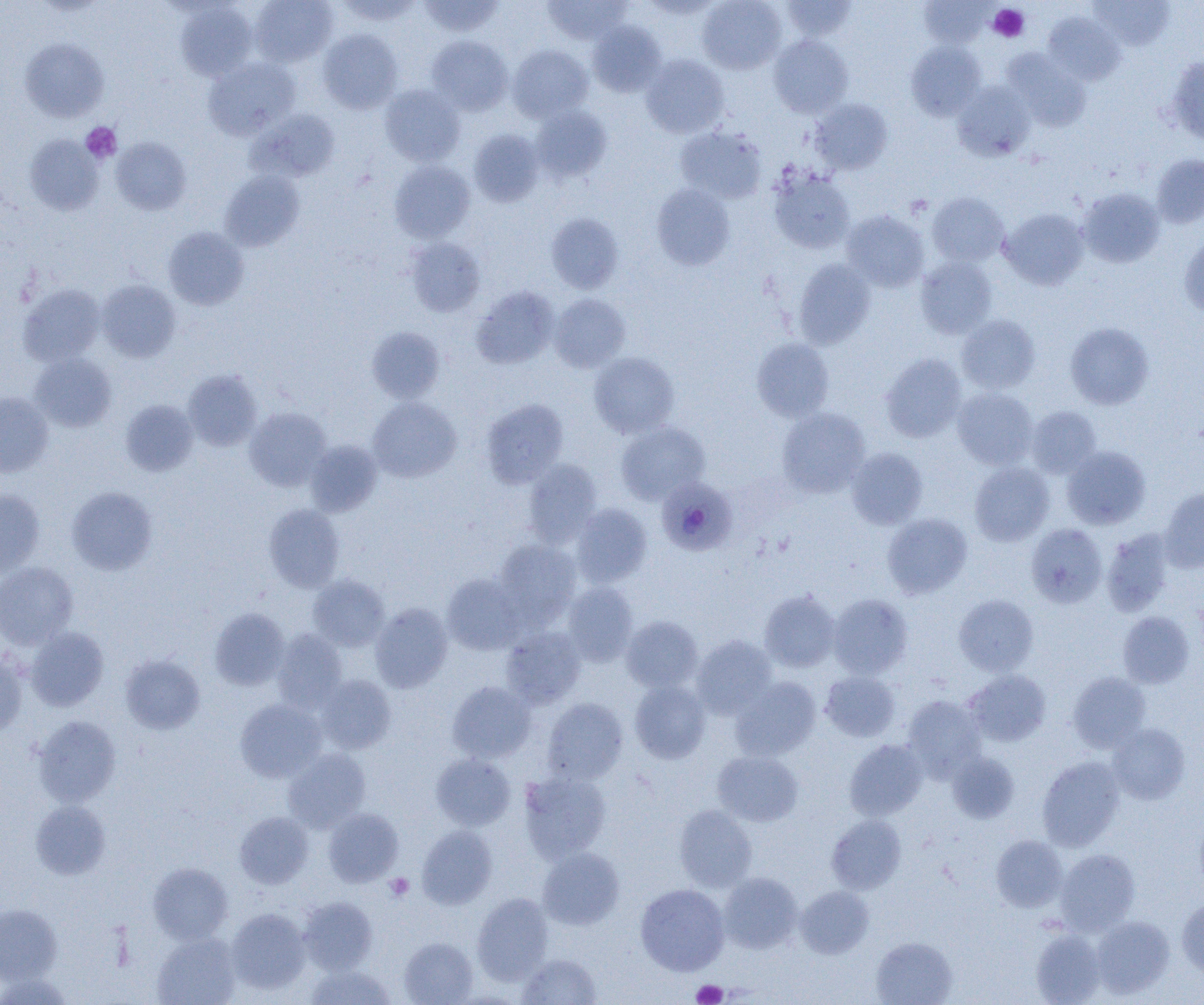
Summary:
  - Coordinate format: approximate bounding boxes as (x1, y1, x2, y2) in pixels
  - Plasmodium malariae-infected red blood cell locations: (657, 478, 737, 556)
  - Platelet locations: (988, 4, 1029, 42), (81, 122, 121, 163), (385, 873, 413, 901), (692, 980, 727, 1004)
  - Uninfected red blood cell locations: (250, 0, 338, 67), (335, 0, 422, 25), (417, 0, 505, 36), (543, 0, 632, 45), (697, 0, 787, 74), (782, 0, 858, 42), (920, 0, 992, 48), (1089, 0, 1174, 50), (175, 2, 258, 81), (1042, 12, 1125, 85), (588, 21, 666, 96), (318, 29, 403, 114), (426, 35, 513, 116), (769, 35, 853, 118), (20, 38, 109, 122), (906, 41, 986, 120), (508, 45, 593, 123), (1002, 49, 1091, 132), (641, 54, 729, 138), (1166, 54, 1204, 145), (204, 56, 301, 140), (952, 81, 1036, 161), (380, 84, 465, 166), (810, 98, 893, 175), (530, 106, 611, 183), (247, 109, 341, 182), (675, 126, 767, 204), (469, 129, 544, 206), (25, 135, 103, 215), (111, 137, 191, 215), (1151, 154, 1204, 228), (389, 161, 475, 243), (768, 169, 855, 254), (219, 170, 305, 252), (651, 183, 735, 270), (1078, 187, 1165, 268), (927, 193, 1009, 267), (999, 208, 1089, 290), (841, 210, 929, 292), (546, 213, 624, 294), (163, 227, 249, 310), (1179, 236, 1204, 317), (406, 238, 485, 317), (915, 256, 998, 339), (793, 258, 876, 348), (97, 280, 180, 363), (18, 284, 105, 366), (471, 285, 559, 369), (549, 293, 631, 372), (956, 314, 1041, 394), (1065, 322, 1154, 410), (366, 326, 446, 403), (751, 337, 834, 422), (30, 352, 116, 432), (589, 352, 680, 438), (880, 353, 967, 442), (183, 370, 263, 451), (952, 387, 1038, 470), (0, 391, 53, 477), (367, 397, 461, 482), (481, 398, 568, 488), (120, 400, 198, 476), (1026, 406, 1102, 478), (244, 407, 331, 491), (776, 407, 870, 498), (616, 422, 710, 504), (305, 439, 382, 516), (1062, 446, 1151, 530), (846, 448, 928, 529), (522, 459, 602, 547), (969, 462, 1054, 546), (67, 487, 157, 574), (1159, 487, 1204, 571), (0, 490, 45, 576), (570, 503, 652, 587), (263, 504, 345, 592), (882, 513, 972, 598), (1025, 523, 1107, 608), (1101, 528, 1175, 616), (494, 539, 581, 626), (0, 562, 78, 649), (441, 573, 527, 655), (308, 574, 390, 651), (562, 582, 638, 667), (759, 591, 840, 672), (828, 593, 912, 679), (953, 594, 1038, 676), (370, 602, 453, 692), (210, 607, 290, 690), (1118, 611, 1195, 688), (621, 615, 703, 693), (501, 626, 586, 709), (25, 627, 108, 711), (273, 629, 348, 712), (691, 635, 778, 718), (0, 651, 27, 735), (120, 654, 205, 734), (963, 669, 1051, 746), (820, 671, 901, 742), (1067, 671, 1151, 753), (316, 675, 396, 754), (730, 677, 821, 761), (630, 680, 711, 763), (447, 681, 536, 763), (903, 695, 986, 778), (541, 697, 628, 784), (235, 699, 326, 782), (33, 715, 121, 807), (1107, 722, 1191, 804), (844, 739, 928, 820), (283, 749, 370, 832), (712, 750, 803, 826), (947, 752, 1020, 823), (431, 753, 516, 830), (1037, 755, 1124, 851), (519, 769, 612, 862), (30, 801, 111, 879), (674, 805, 757, 892), (323, 808, 402, 886), (234, 812, 313, 888), (827, 814, 906, 894), (417, 825, 497, 909), (990, 835, 1068, 912), (537, 847, 625, 930), (1055, 849, 1140, 934), (149, 862, 233, 944), (718, 872, 803, 953), (635, 883, 729, 976), (795, 886, 874, 958), (472, 892, 553, 984), (298, 896, 377, 974), (1176, 898, 1204, 977), (0, 903, 61, 984), (226, 908, 311, 994), (1090, 915, 1174, 998), (1031, 928, 1106, 1005), (152, 933, 241, 1005), (871, 936, 957, 1005), (399, 937, 477, 1004), (517, 953, 602, 1005), (305, 963, 396, 1005)
  - Slide-level diagnosis: Plasmodium malariae
  - Image size: 1204×1005 pixels
  - Magnification: 1000x
  - Modality: optical microscopy
  - Field of view: single
  - Preparation: thin blood smear